Give a bounding box for every artifact (platelet-like body, stain precipitate, or debris).
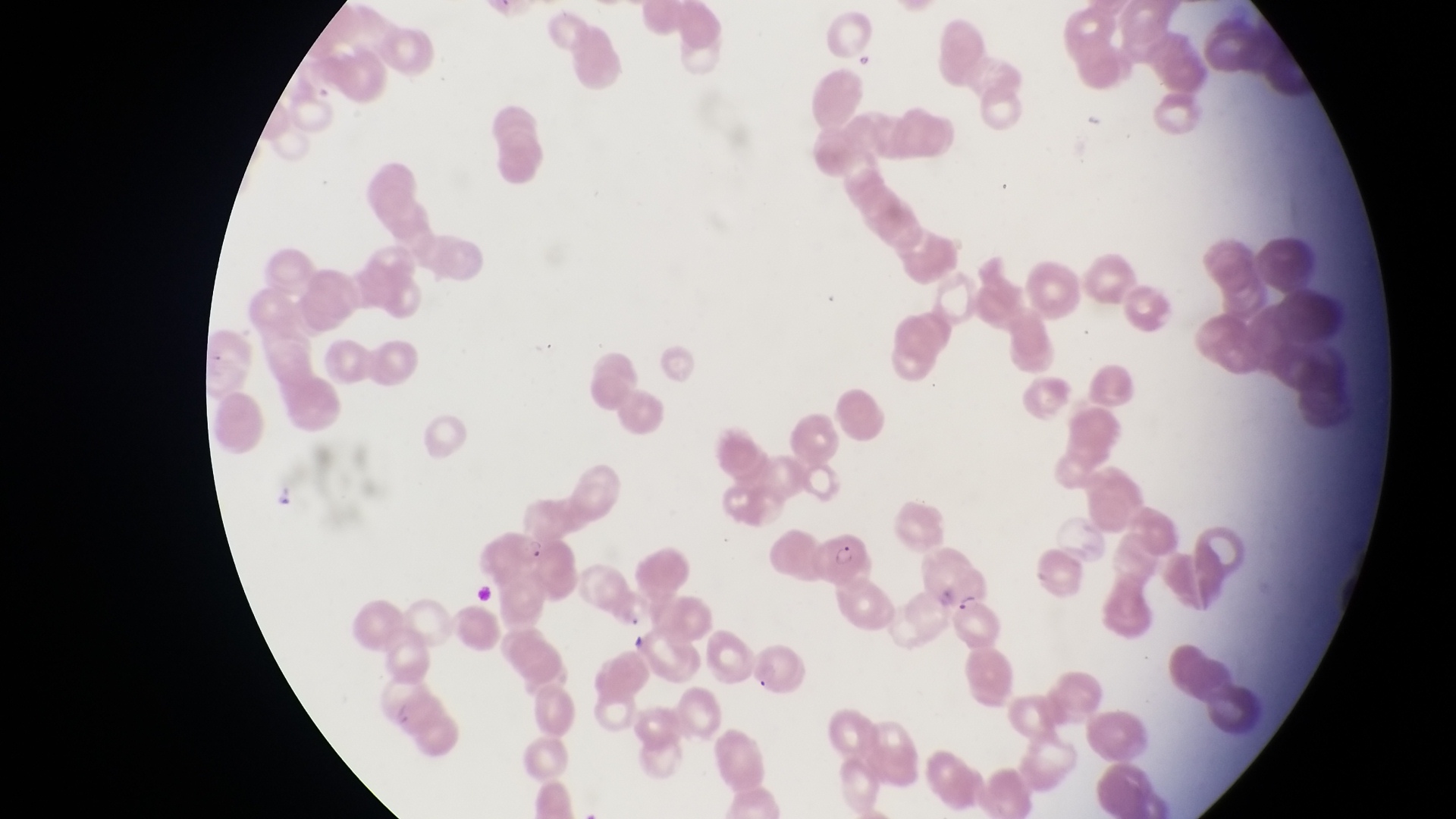

Approximate bounding boxes as [left, top, right, bottom] in pixels.
Artifacts (platelet-like body, stain precipitate, or debris): [851, 50, 884, 74].

Summary:
  - Parasitised red blood cell locations: [812, 526, 873, 585], [943, 563, 993, 613]
  - Trophozoite locations: [270, 476, 294, 506], [522, 531, 545, 563]
  - Image size: 1456×819 pixels
  - Capture: smartphone photograph through the eyepiece of an Olympus CX-23 microscope
  - Country: Uganda
  - Preparation: thin blood smear
  - Field of view: single
  - Magnification: 1000x